Assess the morphology of the erythrocytes.
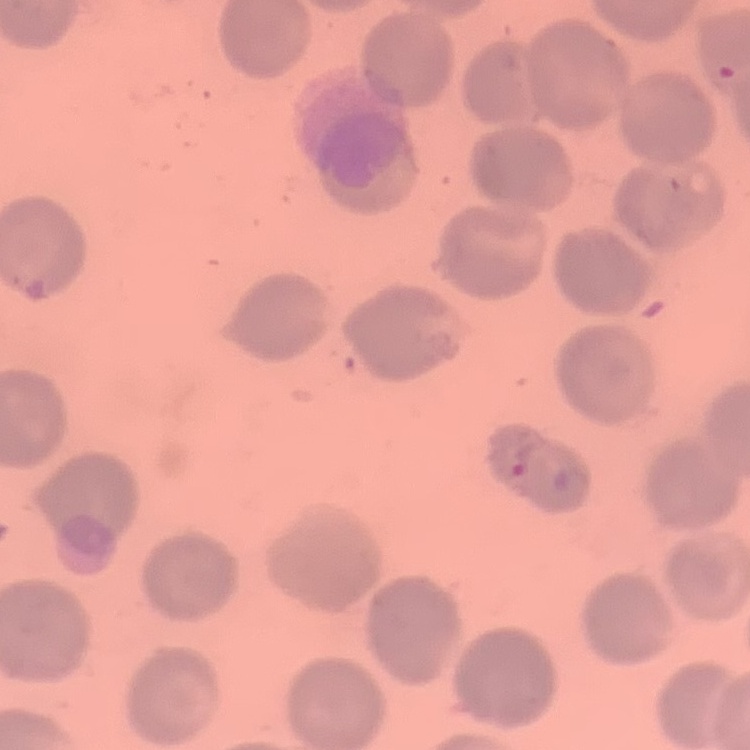

No rouleaux formation.

Summary:
  - Image type: one tile cut from a larger photomicrograph
  - Stain: Field's or Giemsa
  - Preparation: thin blood film